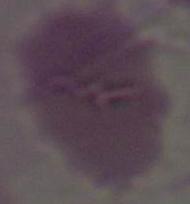 An erythrocyte is shown. Micrograph. 1000x magnification.